Assess this cell for malaria.
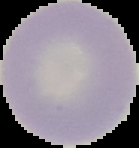

Uninfected.

The area outside the segmented cell region is set to black. From a thin blood smear. Image is 139×148 pixels.